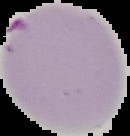
{
  "preparation": "thin blood film",
  "image_type": "segmented cell region on a black background",
  "image_size": "130×136 pixels",
  "result": "malaria parasites identified"
}